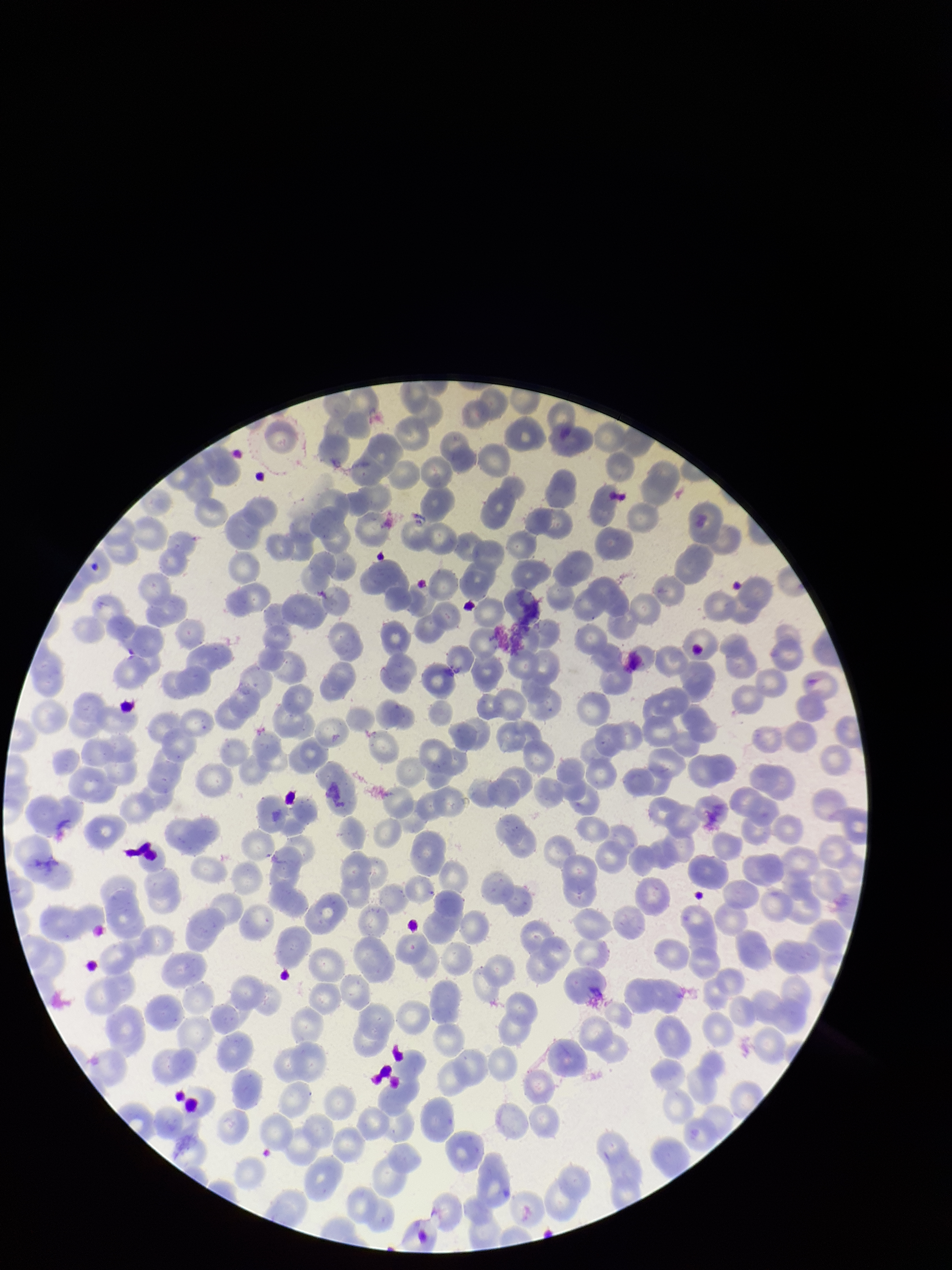 Red blood cell count: 212. Stained with Giemsa. Preparation: thin. Parasitized red blood cells: none detected. Image is 952×1270 pixels. Parasitized red blood cell count: 0. Patient malaria status: positive. Photographed through the microscope eyepiece with a smartphone camera. Single field of view. Species reported for this patient: Plasmodium vivax.